Locate every uninfected red blood cell.
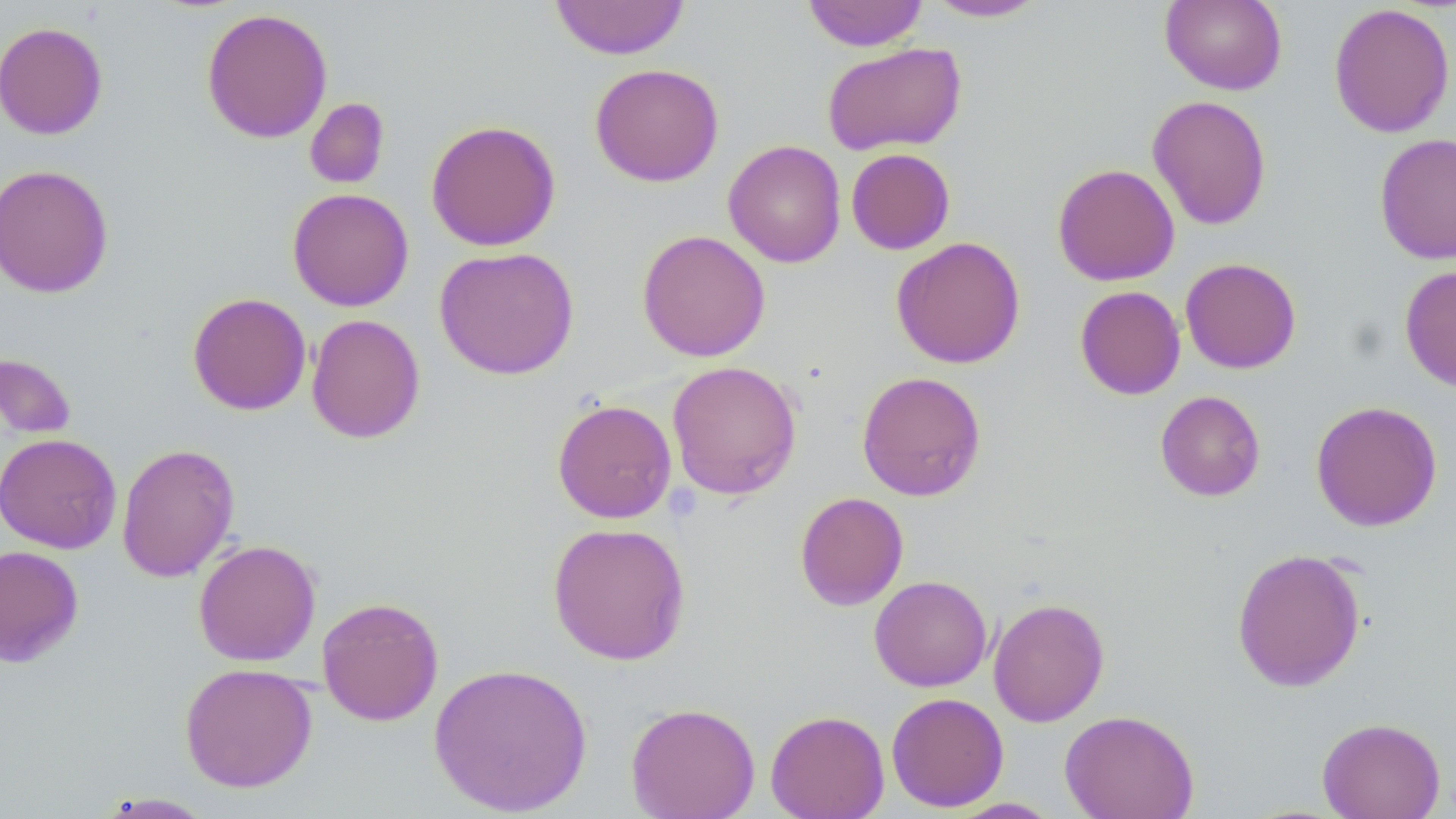

Approximate bounding boxes as [x1, y1, x2, y2] in pixels.
Uninfected red blood cells: [801, 0, 929, 51], [1160, 0, 1287, 95], [549, 1, 691, 60], [923, 1, 1050, 22], [1329, 3, 1455, 138], [200, 7, 333, 144], [0, 21, 108, 140], [822, 41, 967, 156], [589, 63, 724, 187], [1147, 95, 1272, 230], [304, 97, 390, 189], [425, 118, 561, 252], [1374, 132, 1456, 264], [723, 140, 846, 268], [846, 148, 955, 254], [1052, 163, 1180, 286], [0, 164, 114, 298], [287, 188, 414, 311], [637, 230, 771, 362], [891, 236, 1026, 369], [434, 246, 580, 380], [1180, 257, 1302, 374], [1399, 264, 1456, 392], [1074, 285, 1186, 400], [187, 292, 312, 416], [306, 314, 426, 444], [0, 351, 77, 441], [666, 360, 803, 500], [856, 371, 987, 501], [1155, 390, 1266, 501], [551, 399, 677, 524], [1310, 400, 1443, 532], [0, 432, 122, 554], [116, 443, 240, 582], [794, 491, 909, 611], [547, 521, 692, 665], [193, 539, 321, 667], [0, 544, 84, 668], [1231, 548, 1366, 693], [869, 575, 992, 692], [869, 586, 1109, 702], [316, 596, 444, 726], [988, 596, 1109, 727], [428, 661, 593, 816], [179, 662, 318, 793], [886, 692, 1009, 812], [625, 702, 760, 819], [765, 709, 890, 819], [1060, 709, 1199, 819], [1317, 716, 1446, 819], [95, 792, 219, 818], [947, 797, 1062, 818].

slide_level_diagnosis: negative for blood parasites
stain: May-Grünwald-Giemsa
preparation: thin blood smear
image_size: 1456×819 pixels
field_of_view: single
magnification: 1000x
modality: light microscopy